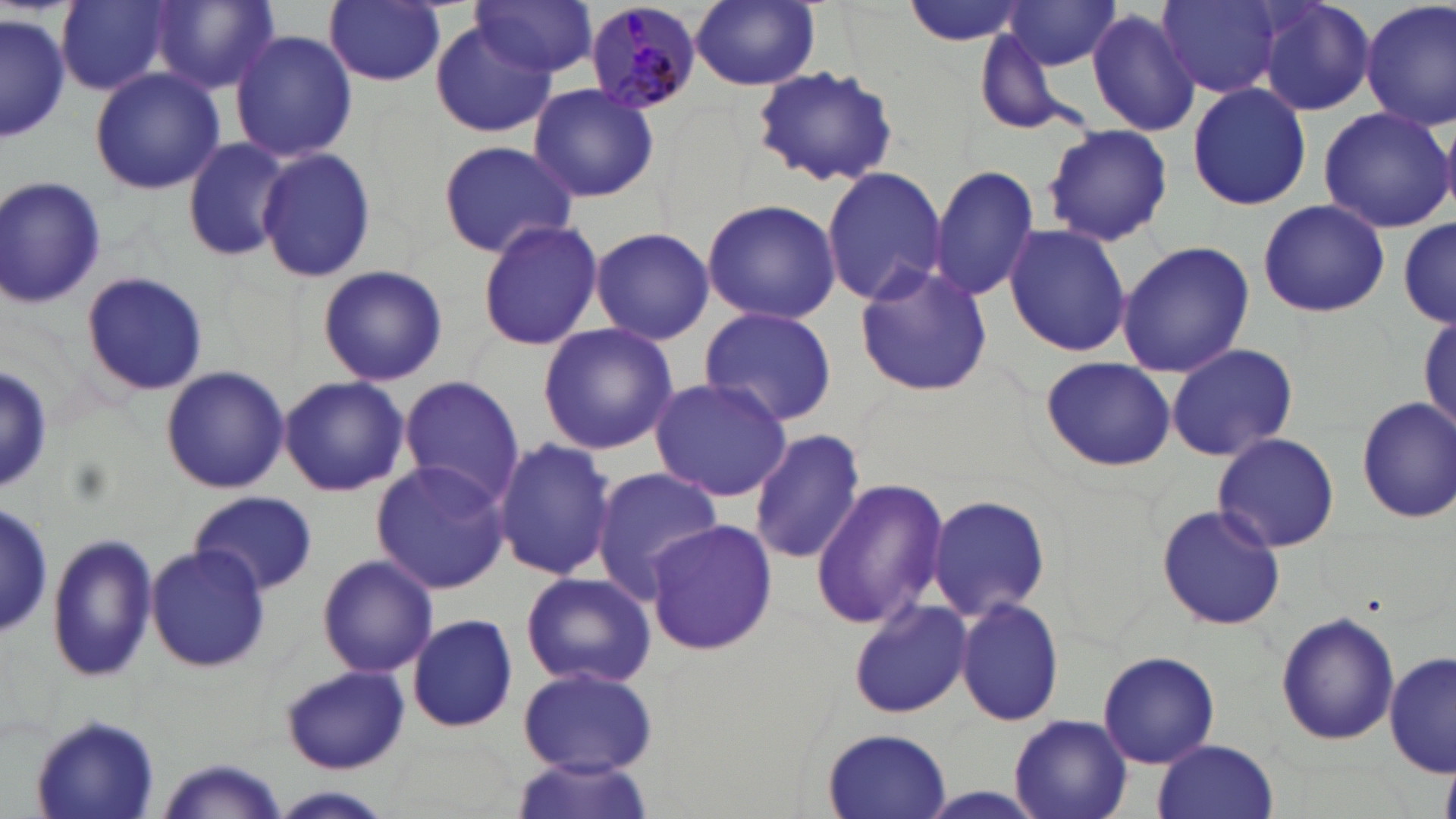
slide_level_diagnosis: Plasmodium malariae
stain: May-Grünwald-Giemsa
magnification: 1000x
preparation: thin blood film
image_size: 1456×819 pixels
modality: light microscopy
plasmodium_malariae_infected_red_blood_cell_locations: 'approximate bounding boxes as (x1, y1, x2, y2) in pixels: (583, 2, 704, 113)'
uninfected_red_blood_cell_locations: 'approximate bounding boxes as (x1, y1, x2, y2) in pixels: (56, 0, 172, 95), (473, 0, 596, 78), (691, 0, 820, 90), (900, 0, 1035, 46), (1001, 0, 1123, 72), (1156, 0, 1284, 97), (1254, 0, 1377, 117), (147, 1, 279, 95), (326, 1, 445, 87), (1361, 1, 1456, 131), (1085, 6, 1201, 138), (0, 12, 71, 140), (431, 24, 554, 138), (230, 28, 358, 162), (972, 28, 1084, 133), (751, 65, 899, 187), (90, 66, 224, 194), (1186, 81, 1313, 211), (527, 83, 659, 205), (1317, 105, 1455, 234), (1042, 123, 1173, 247), (180, 137, 293, 263), (437, 140, 579, 259), (255, 147, 376, 285), (929, 163, 1041, 302), (820, 167, 948, 305), (0, 173, 106, 310), (1257, 198, 1389, 318), (700, 199, 842, 323), (477, 219, 602, 351), (1396, 219, 1454, 330), (1003, 224, 1133, 358), (591, 226, 715, 346), (1115, 240, 1254, 378), (317, 264, 447, 387), (852, 264, 993, 396), (80, 270, 210, 397), (698, 306, 838, 428), (1418, 312, 1454, 439), (538, 322, 677, 454), (1165, 342, 1299, 462), (1039, 356, 1175, 471), (159, 366, 290, 495), (278, 375, 409, 497), (398, 375, 522, 503), (648, 375, 793, 501), (1356, 395, 1456, 525), (750, 427, 869, 565), (1212, 431, 1341, 553), (492, 438, 619, 583), (370, 459, 512, 593), (590, 466, 724, 602), (811, 477, 950, 630), (189, 490, 318, 596), (925, 492, 1051, 622), (0, 495, 51, 643), (1156, 502, 1285, 632), (643, 520, 777, 654), (45, 531, 156, 684), (146, 544, 270, 673), (316, 554, 438, 679), (520, 570, 657, 689), (955, 595, 1065, 726), (847, 600, 972, 719), (1276, 610, 1398, 746), (407, 612, 518, 733), (1097, 649, 1220, 769), (1385, 650, 1455, 777), (281, 665, 410, 775), (517, 666, 658, 775), (31, 711, 162, 818), (1008, 715, 1134, 819), (820, 726, 955, 818), (1153, 739, 1280, 819), (509, 757, 654, 819), (158, 759, 290, 818), (264, 787, 395, 818)'
field_of_view: single